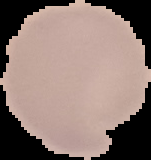
Summary:
  - Result: negative for Plasmodium parasites
  - Image size: 151×160 pixels
  - Image type: cell region segmented out of the field of view; surrounding area masked to black
  - Preparation: thin blood smear